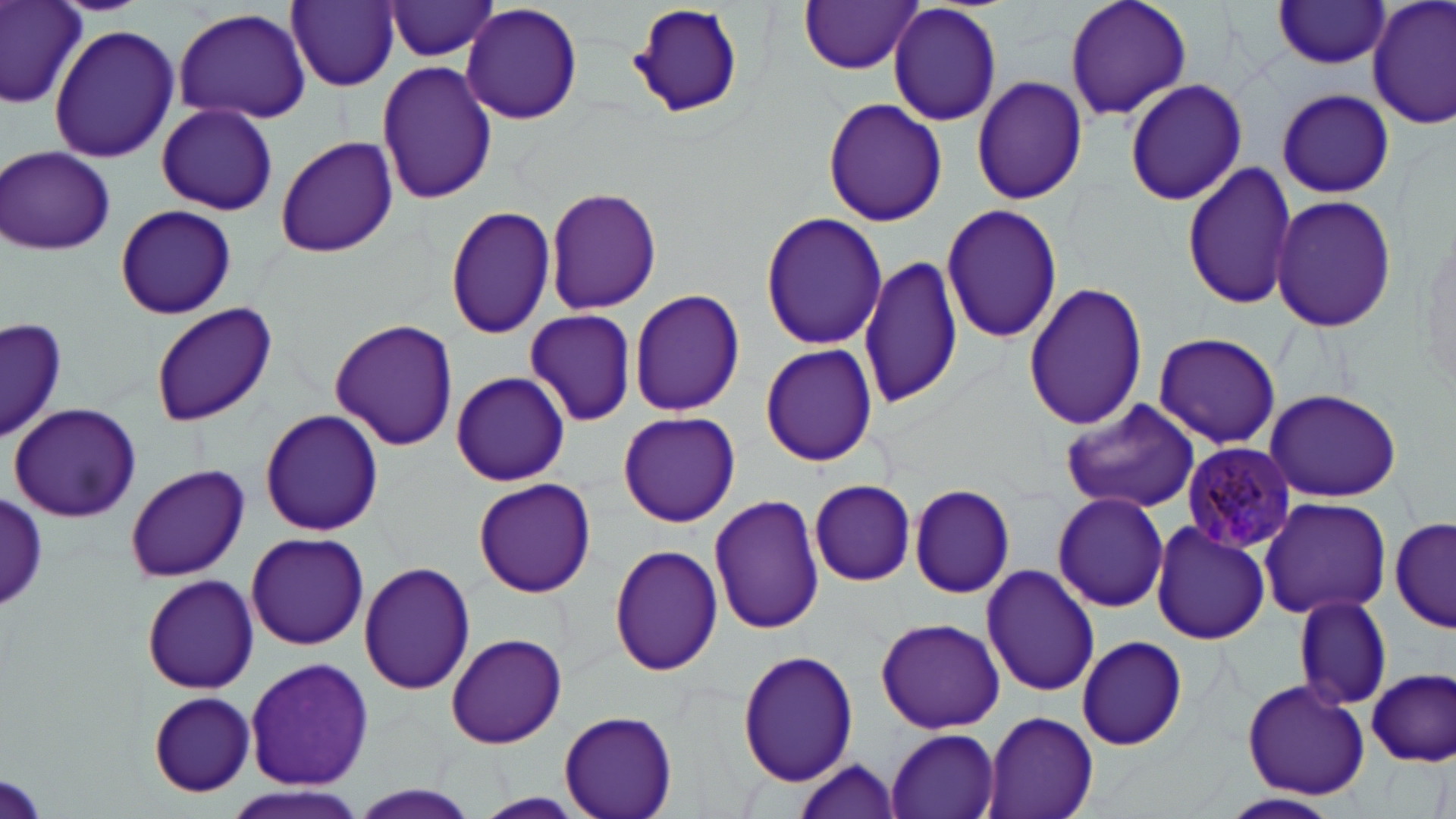
Approximate bounding boxes as (x1, y1, x2, y2) in pixels. Uninfected red blood cell locations: (0, 0, 90, 108), (287, 0, 400, 91), (625, 0, 747, 124), (1063, 0, 1191, 121), (1368, 0, 1455, 131), (383, 1, 501, 61), (800, 1, 923, 75), (887, 1, 1003, 127), (1272, 1, 1392, 70), (460, 4, 584, 124), (172, 7, 311, 125), (48, 23, 180, 164), (376, 59, 499, 204), (971, 76, 1088, 206), (1123, 78, 1247, 207), (1276, 89, 1394, 198), (822, 98, 948, 227), (153, 103, 282, 214), (275, 135, 399, 259), (1, 145, 117, 257), (1180, 160, 1299, 313), (545, 186, 663, 316), (1270, 194, 1397, 333), (940, 203, 1063, 345), (114, 204, 236, 319), (445, 206, 556, 338), (760, 210, 887, 351), (858, 253, 963, 410), (1024, 280, 1148, 431), (628, 287, 746, 417), (149, 304, 276, 427), (524, 310, 637, 426), (0, 315, 66, 446), (330, 317, 459, 451), (1151, 333, 1283, 450), (759, 343, 879, 466), (451, 371, 571, 487), (1262, 389, 1403, 502), (1061, 397, 1204, 515), (9, 401, 143, 523), (259, 409, 384, 537), (615, 411, 741, 527), (123, 463, 250, 582), (472, 477, 596, 598), (809, 478, 917, 586), (742, 483, 859, 605), (908, 483, 1016, 598), (1051, 492, 1170, 613), (709, 494, 826, 634), (2, 496, 47, 607), (1258, 496, 1392, 619), (1390, 513, 1455, 634), (1154, 514, 1386, 638), (1150, 524, 1272, 645), (245, 533, 369, 650), (608, 543, 724, 676), (358, 562, 476, 694), (981, 563, 1100, 697), (141, 574, 259, 694), (1293, 594, 1392, 711), (875, 616, 1006, 734), (446, 632, 566, 748), (1076, 634, 1188, 751), (737, 648, 859, 786), (244, 656, 374, 794), (1368, 670, 1454, 766), (1240, 680, 1370, 798), (147, 692, 256, 796), (982, 709, 1100, 819), (559, 710, 677, 819), (885, 727, 1002, 819), (791, 756, 904, 819), (0, 769, 50, 819), (223, 783, 370, 819), (348, 786, 480, 819), (1223, 792, 1341, 817). Plasmodium malariae-infected red blood cell locations: (1179, 439, 1299, 554). Slide-level diagnosis: Plasmodium malariae. May-Grünwald-Giemsa-stained preparation. Image is 1456×819 pixels. Light microscopy. Captured at 1000x magnification. Thin blood smear. One field of a larger specimen.